Report the malaria status of this cell.
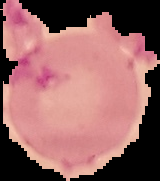

It is uninfected.

preparation: thin blood film
image_size: 160×181 pixels
image_type: segmented cell region on a black background